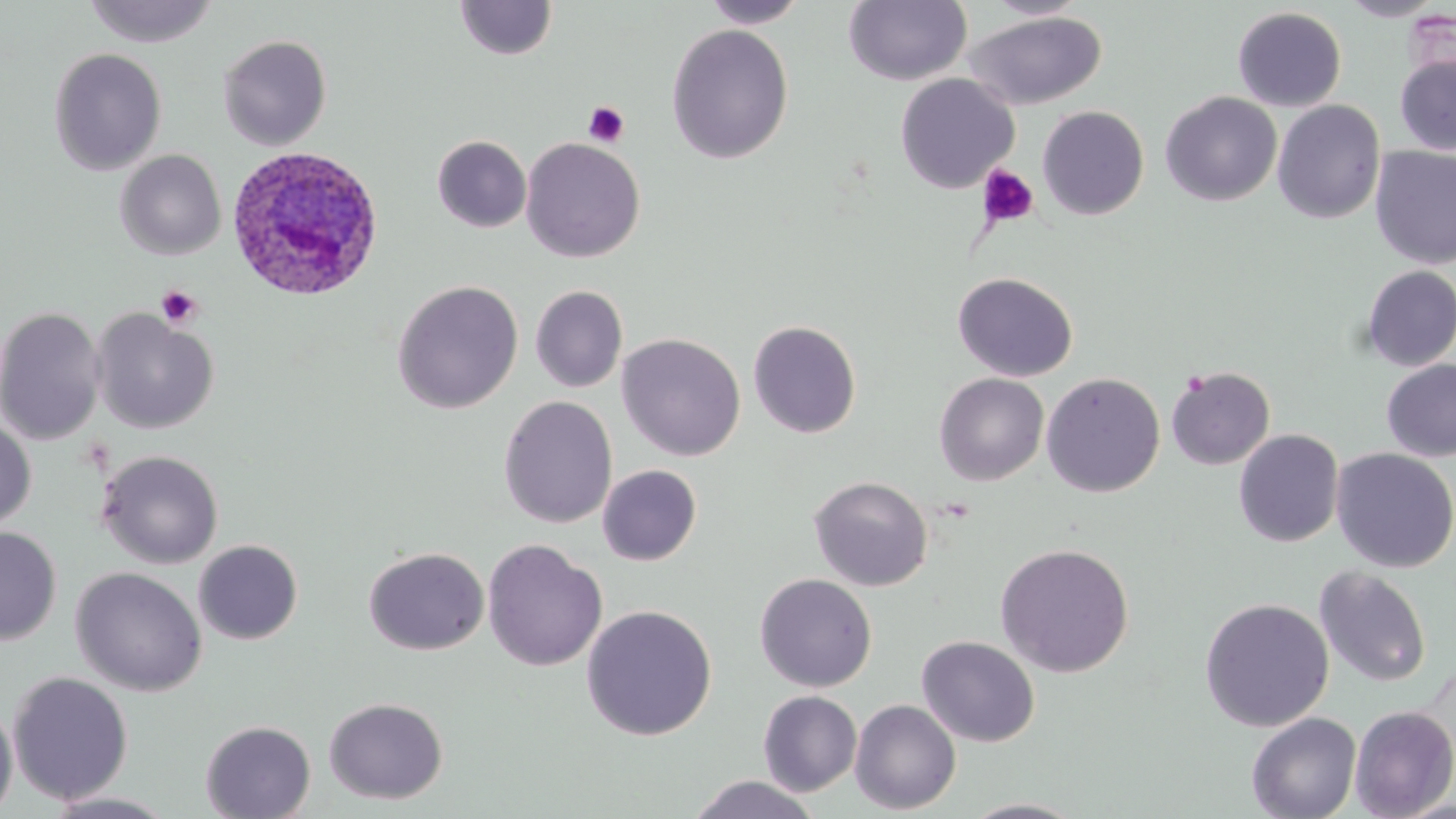
Approximate bounding boxes as [x1, y1, x2, y2] in pixels. Platelet locations: [582, 101, 630, 147], [977, 164, 1040, 230], [156, 285, 201, 329]. Uninfected red blood cell locations: [83, 0, 219, 48], [454, 0, 558, 60], [701, 0, 808, 28], [843, 0, 972, 86], [1336, 0, 1449, 21], [983, 1, 1092, 20], [1232, 7, 1347, 111], [965, 12, 1107, 110], [666, 24, 794, 164], [217, 34, 332, 151], [48, 48, 167, 176], [1394, 53, 1456, 156], [895, 73, 1020, 193], [1160, 91, 1282, 206], [1272, 100, 1386, 224], [1037, 105, 1149, 220], [432, 135, 531, 233], [520, 137, 645, 263], [1370, 145, 1456, 269], [115, 149, 227, 260], [1359, 265, 1456, 371], [953, 272, 1078, 382], [391, 279, 524, 414], [530, 285, 628, 393], [0, 305, 106, 447], [91, 309, 218, 434], [748, 319, 862, 438], [616, 333, 746, 461], [1381, 359, 1456, 462], [1165, 365, 1276, 470], [934, 372, 1049, 485], [1042, 372, 1165, 498], [498, 395, 617, 528], [0, 416, 36, 533], [1234, 429, 1344, 547], [1330, 448, 1456, 573], [96, 449, 224, 569], [597, 464, 702, 566], [809, 475, 933, 592], [0, 526, 61, 646], [482, 539, 607, 672], [193, 540, 303, 645], [994, 542, 1135, 677], [363, 546, 490, 655], [70, 566, 208, 697], [1314, 566, 1432, 688], [754, 573, 878, 692], [1199, 597, 1335, 732], [581, 604, 717, 741], [917, 635, 1040, 747], [7, 671, 134, 806], [758, 690, 862, 796], [0, 697, 18, 818], [324, 697, 448, 804], [850, 699, 961, 814], [1349, 705, 1456, 818], [1246, 712, 1361, 819], [198, 714, 447, 811], [200, 720, 316, 819], [686, 774, 823, 818], [39, 791, 180, 818], [959, 798, 1088, 818]. Plasmodium ovale-infected red blood cell locations: [223, 145, 384, 303]. Slide-level diagnosis: Plasmodium ovale. Thin blood film. 1000x magnification. May-Grünwald-Giemsa-stained preparation. Light microscopy. Image is 1456×819 pixels. One field of a larger specimen.